Assess this cell for malaria.
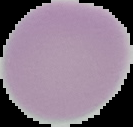

It is uninfected.

preparation = thin blood film
image type = segmented cell region on a black background
image size = 133×127 pixels